Locate every Plasmodium parasite.
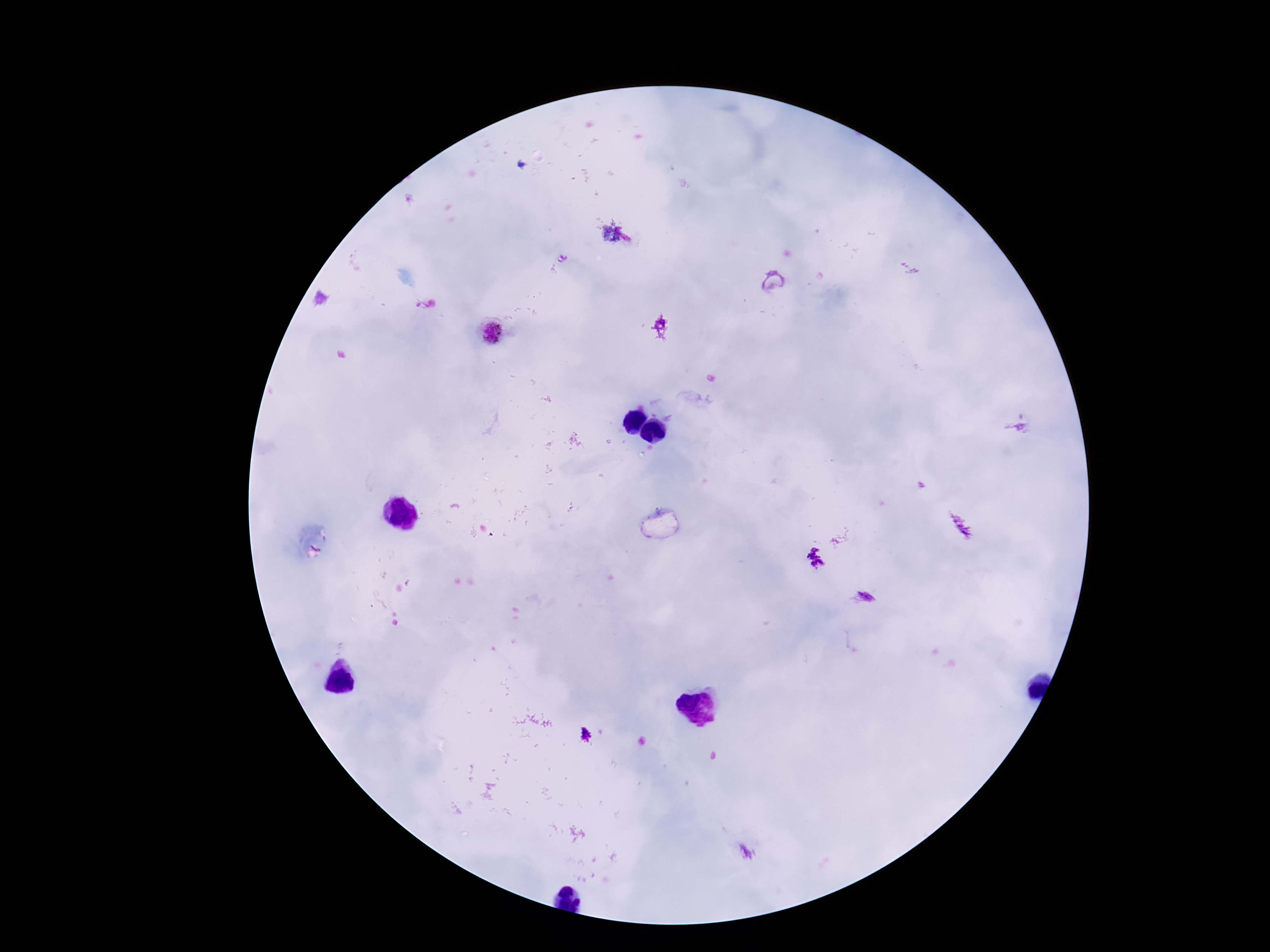

Approximate object centers, in pixels from the top-left corner.
Plasmodium parasites: (x=773, y=280), (x=662, y=327), (x=490, y=332), (x=865, y=596).

preparation = thick peripheral-blood smear
field of view = one from this slide
capture = smartphone camera through the microscope eyepiece
magnification = 100x
stain = Giemsa
patient malaria status = positive
image size = 1270×952 pixels